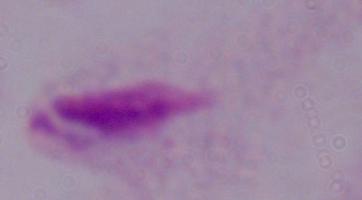
A trichomonad is seen. Photomicrograph. Captured at 1000x magnification.